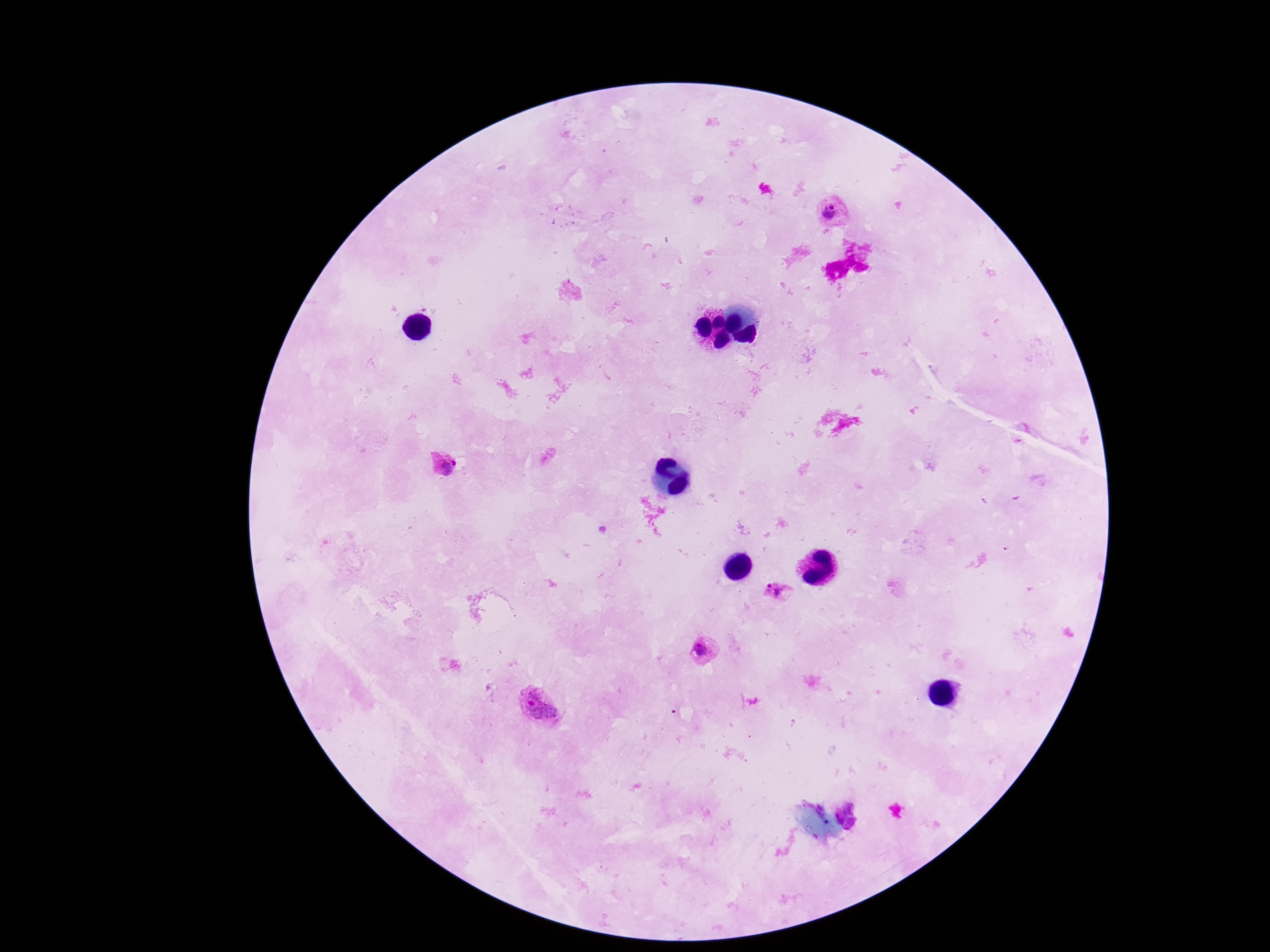 Approximate centers as {x, y} in pixels. Plasmodium parasite locations: {832, 212}, {445, 465}, {781, 594}, {707, 653}, {539, 710}, {851, 815}. Giemsa-stained preparation. Thick blood film. Image is 1270×952 pixels. One field from this slide. Patient malaria status: infected. Photographed through the microscope eyepiece with a smartphone camera. 100x magnification.